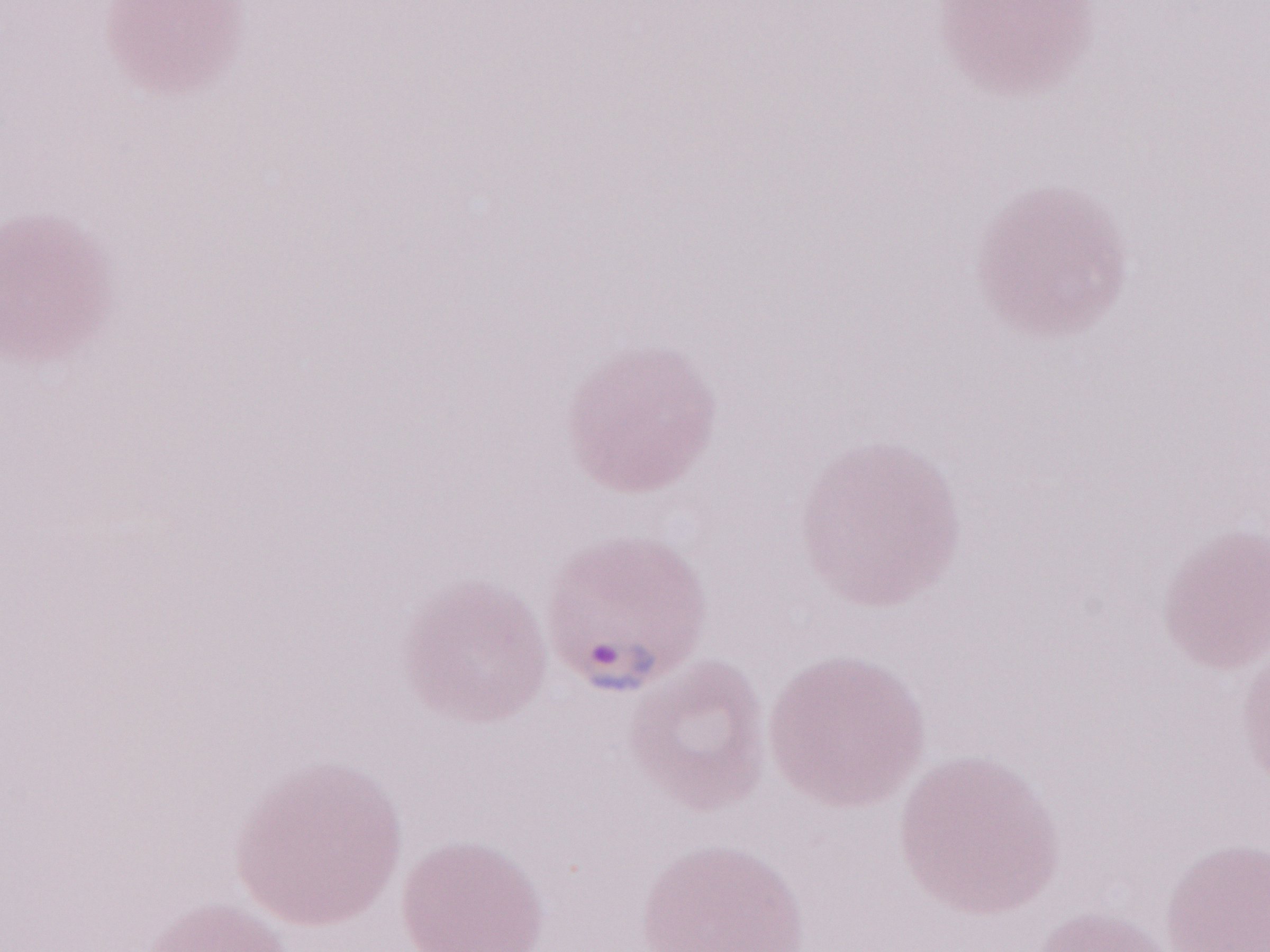 May-Grünwald-Giemsa-stained preparation. Single field of view. Olympus BX43 microscope, Olympus DP73 camera. Thin blood film. Patient-level malaria diagnosis: positive. Magnification: 1,000x. Image is 1270×952 pixels.